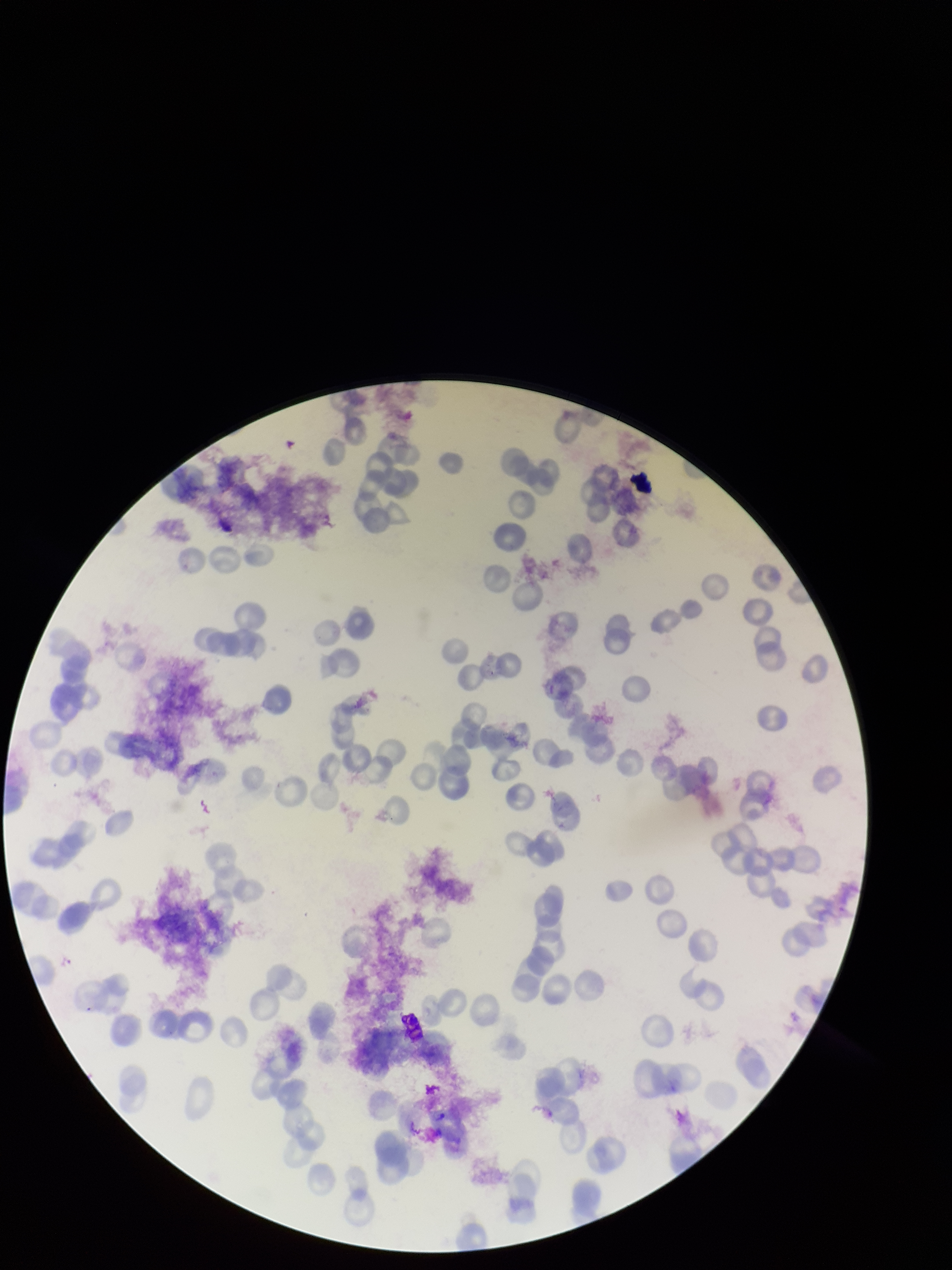

preparation = thin
red blood cell count = 122
patient malaria status = positive
field of view = one from this slide
stain = Giemsa
species reported for this patient = Plasmodium vivax
image size = 952×1270 pixels
parasitized red blood cell count = 0
parasitized red blood cells = none seen
capture = smartphone photograph through the microscope eyepiece